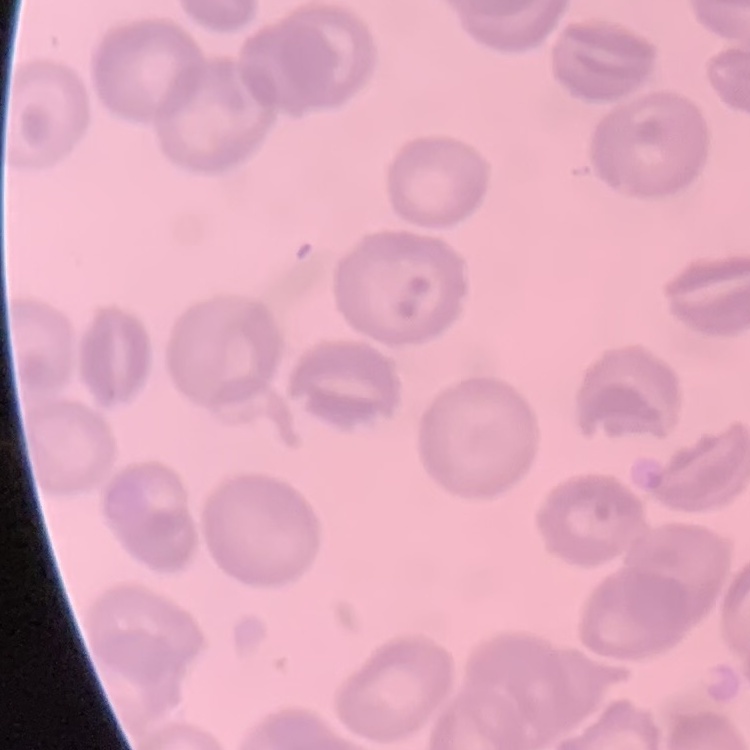

erythrocyte morphology = no rouleaux formation
preparation = thin blood film
image type = square crop of a larger photomicrograph
stain = Field's or Giemsa